Assess the morphology of the erythrocytes.
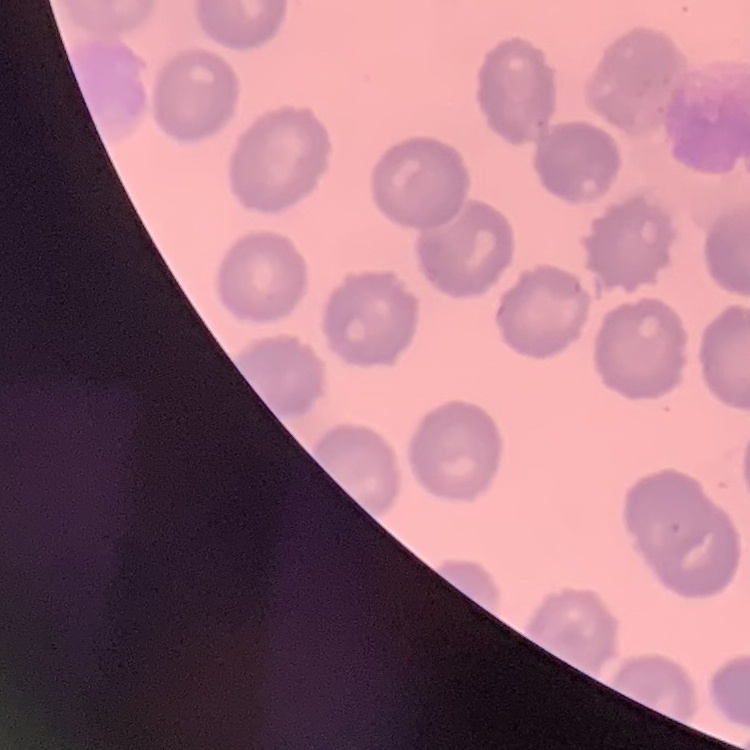

No rouleaux formation.

Square crop of a larger photomicrograph. Thin blood film. Stained with either Field's or Giemsa.